Classify the preparation.
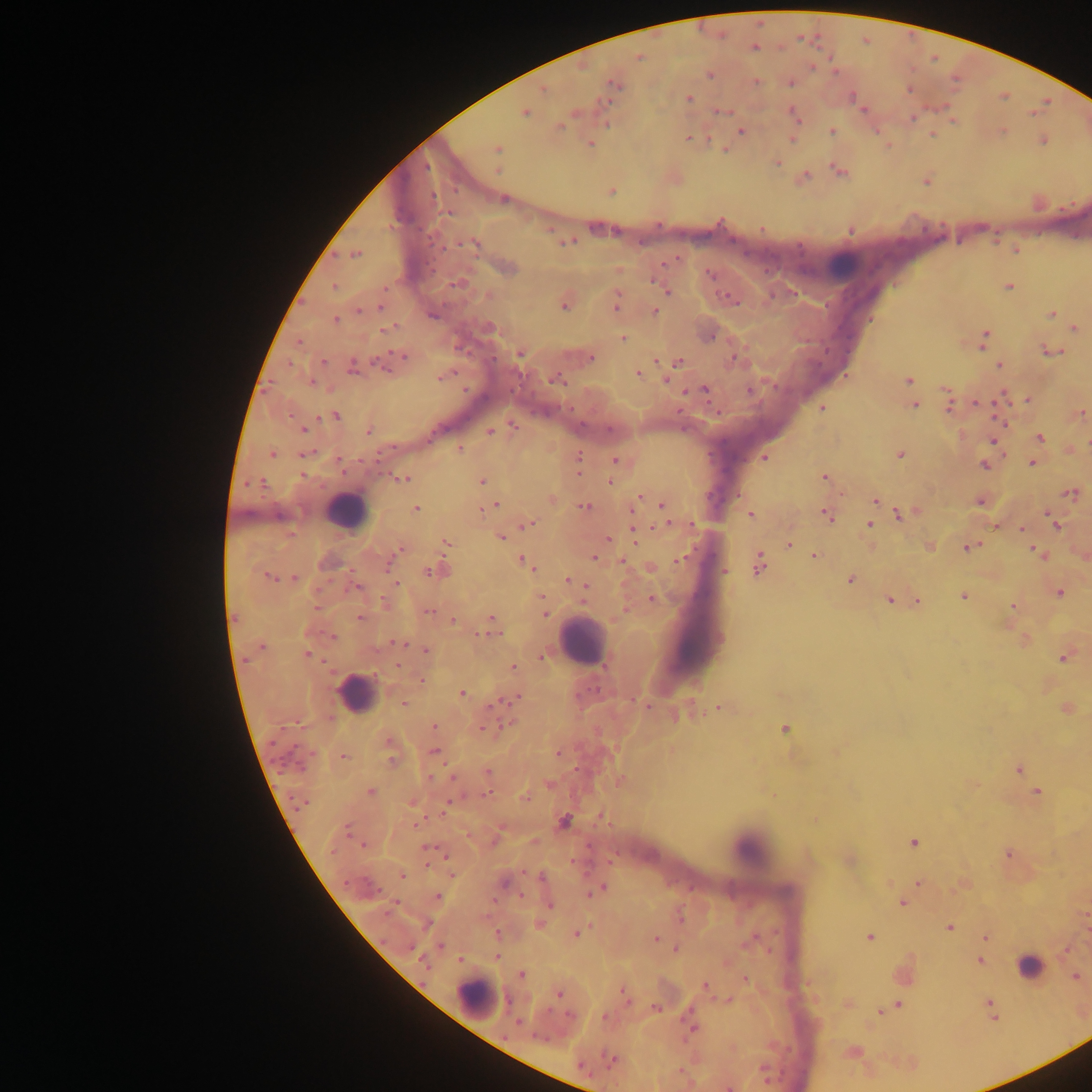
Thick blood film.

Approximate centers as [x, y] in pixels. Plasmodium parasite locations: [755, 47], [639, 56], [812, 66], [710, 75], [757, 82], [790, 83], [614, 84], [544, 89], [909, 89], [689, 98], [604, 101], [863, 110], [722, 111], [525, 112], [793, 114], [912, 117], [559, 128], [741, 131], [832, 131], [932, 135], [688, 138], [793, 139], [1043, 141], [591, 144], [497, 149], [778, 162], [498, 170], [838, 170], [611, 192], [504, 198], [567, 242], [471, 244], [1014, 251], [356, 254], [653, 280], [458, 283], [335, 286], [659, 286], [1009, 287], [667, 291], [730, 298], [616, 304], [564, 306], [381, 307], [359, 311], [655, 312], [1051, 314], [433, 316], [335, 320], [1075, 328], [388, 330], [984, 337], [623, 339], [1052, 352], [520, 354], [402, 356], [591, 358], [680, 361], [323, 362], [380, 364], [353, 366], [1000, 366], [638, 373], [443, 376], [557, 379], [666, 380], [909, 380], [312, 382], [704, 390], [749, 390], [1027, 399], [978, 403], [915, 405], [949, 408], [822, 409], [1082, 413], [336, 416], [513, 425], [303, 430], [369, 431], [490, 431], [1040, 438], [992, 441], [460, 450], [272, 454], [305, 454], [900, 454], [764, 458], [615, 460], [339, 461], [578, 462], [1031, 464], [985, 465], [824, 478], [403, 479], [482, 481], [610, 481], [255, 483], [1072, 493], [553, 499], [875, 500], [979, 503], [661, 504], [494, 506], [585, 506], [415, 508], [751, 515], [826, 515], [900, 516], [1054, 523], [528, 525], [666, 525], [869, 525], [996, 526], [1022, 529], [634, 532], [501, 538], [608, 538], [446, 542], [789, 544], [931, 546], [968, 547], [400, 550], [1036, 552], [815, 556], [594, 558], [524, 561], [622, 561], [390, 563], [758, 565], [650, 569], [430, 572], [268, 576], [294, 578], [850, 579], [568, 581], [396, 583], [583, 585], [356, 587], [1060, 593], [964, 597], [652, 599], [889, 600], [918, 601], [1013, 606], [316, 607], [428, 612], [545, 614], [360, 618], [453, 620], [492, 621], [492, 629], [334, 636], [395, 642], [261, 647], [424, 649], [307, 655], [542, 657], [1063, 658], [398, 665], [513, 667], [422, 680], [463, 694], [516, 699], [404, 703], [647, 707], [719, 708], [677, 716], [434, 726], [483, 728], [784, 730], [435, 751], [558, 754], [344, 757], [391, 758], [1019, 769], [488, 772], [431, 777], [549, 784], [370, 792], [1036, 792], [525, 797], [299, 802], [447, 807], [600, 816], [564, 822], [417, 824], [346, 829], [913, 842], [363, 846], [428, 847], [1008, 854], [402, 876], [541, 876], [918, 883], [599, 889], [521, 895], [438, 896], [903, 903], [549, 905], [949, 928], [576, 934], [870, 937], [985, 937], [655, 939], [411, 947], [441, 947], [676, 950], [497, 956], [980, 961], [422, 963], [522, 975], [1075, 977], [745, 979], [705, 985], [625, 993], [559, 994], [989, 1003], [899, 1004], [656, 1009], [880, 1011], [604, 1017], [518, 1022], [691, 1027], [613, 1059], [581, 1065], [728, 1088]. Leukocyte locations: [845, 264], [345, 511], [580, 640], [356, 692], [749, 847], [1032, 968], [476, 997]. Single field of view. Sample from Ghana. Image is 1092×1092 pixels. Photographed through a microscope with a mobile-phone camera.